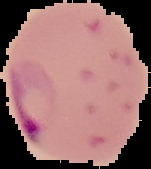
Summary:
  - Preparation: thin blood smear
  - Result: malaria parasites detected
  - Image type: segmented cell region on a black background
  - Image size: 151×169 pixels